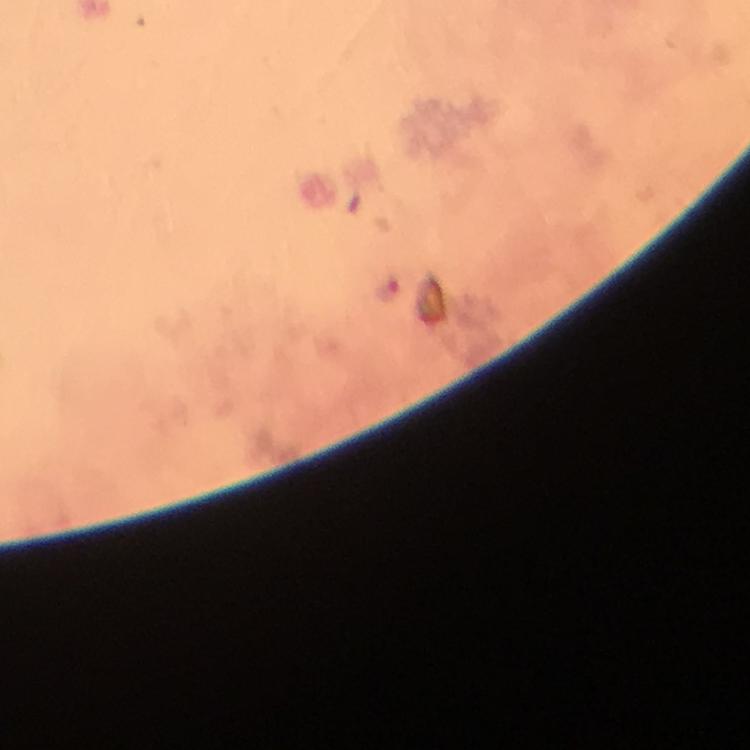

Approximate centers as {x, y} in pixels. Plasmodium parasite locations: {387, 290}. Giemsa-stained preparation. Immersion oil was used. Image is 750×750 pixels. 100x magnification. Thick blood film. From a malaria diagnostic workup. A crop from one field of view. Smartphone photograph taken through a microscope.